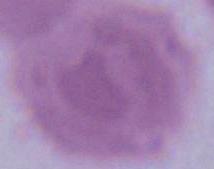
magnification = 1000x
modality = micrograph
identification = erythrocyte